Identify the parasite.
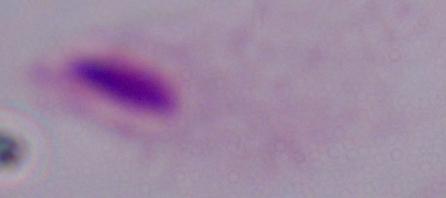
A trichomonad.

magnification = 1000x
modality = micrograph